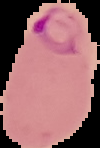
Summary:
  - Preparation: thin blood smear
  - Image size: 100×148 pixels
  - Image type: segmented cell region with the area outside set to black
  - Malaria status: parasitized